Locate every Plasmodium parasite and every leukocyte.
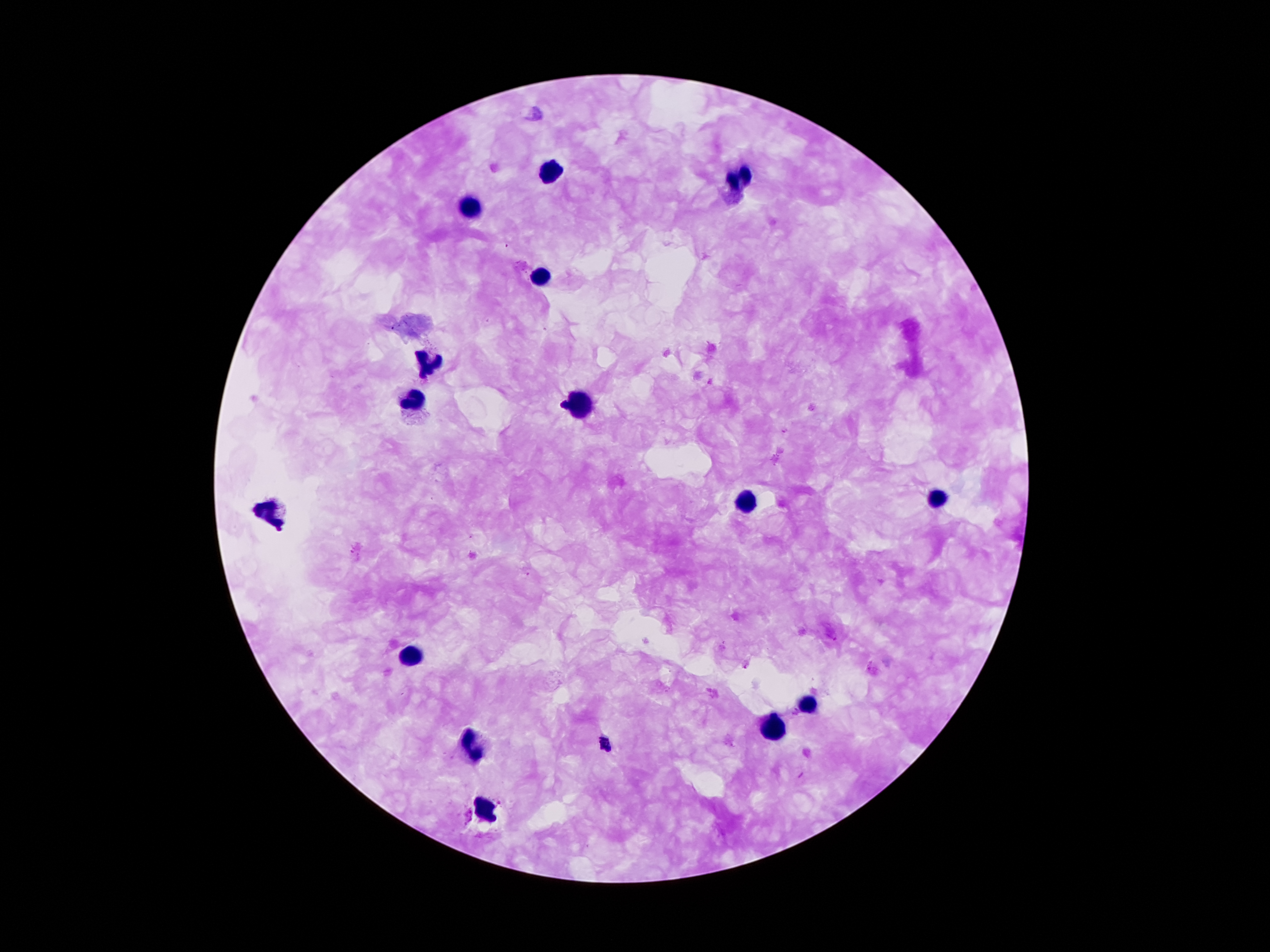
Approximate centers as (x, y) in pixels.
Plasmodium parasites: (562, 406), (604, 740).
Leukocytes: (551, 172), (740, 179), (470, 206), (537, 275), (428, 367), (409, 400), (581, 403), (938, 496), (745, 503), (266, 512), (408, 654), (805, 702), (775, 731), (470, 748), (486, 810).

Image is 1270×952 pixels. Thick peripheral-blood smear. 100x magnification. Giemsa stain. Photographed through the microscope eyepiece with a smartphone camera. Patient malaria status: positive for Plasmodium falciparum. Single field of view.